Assess this cell for malaria.
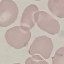

Uninfected.

Thin blood smear. Giemsa stain. Cell patch, automatically extracted from a larger field of view and resized to 64 × 64 pixels. Acquired by smartphone through the microscope eyepiece.